Assess for malaria.
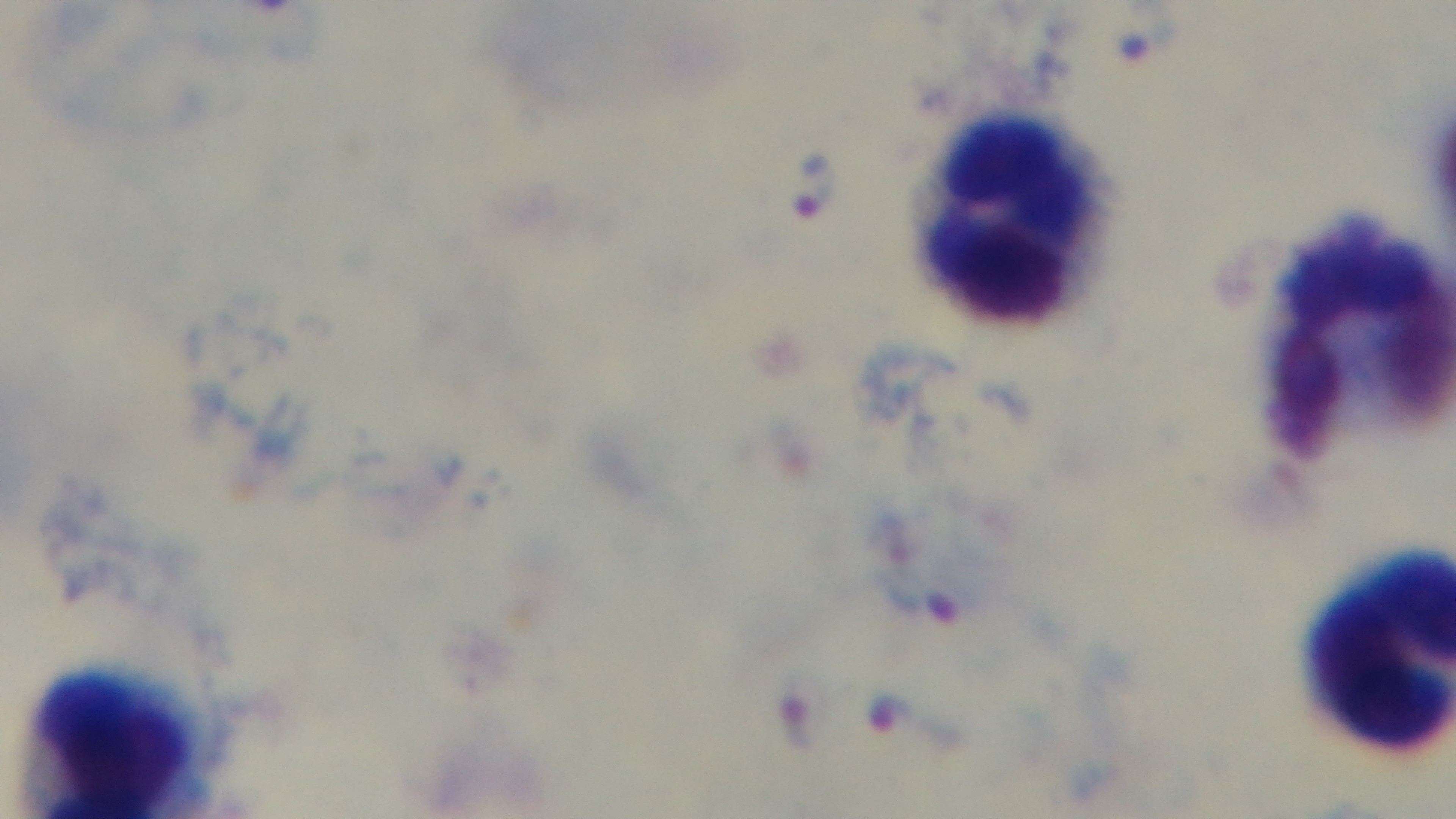
Positive.

field_of_view: one from the slide
objective: 100x oil immersion
preparation: thick blood film
capture: mounted 4K digital camera
stain: Giemsa
modality: light microscopy